Identify the parasite.
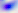

Toxoplasma gondii.

400x magnification. Micrograph.